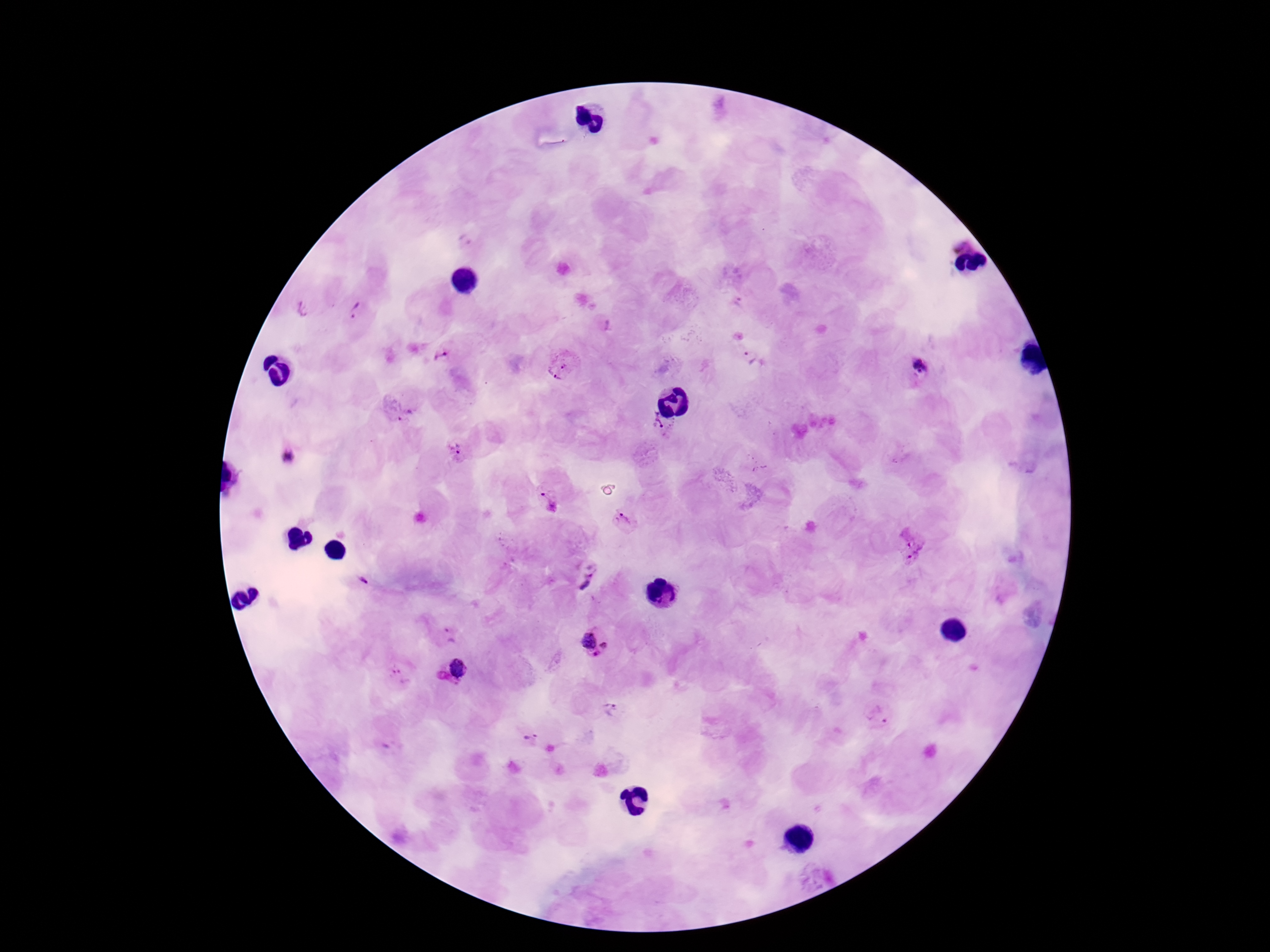 Approximate object centers, in pixels from the top-left corner. Plasmodium parasite locations: (x=357, y=312), (x=442, y=356), (x=753, y=358), (x=561, y=368), (x=920, y=369), (x=398, y=408), (x=659, y=426), (x=458, y=450), (x=288, y=457), (x=548, y=499), (x=625, y=521), (x=908, y=544), (x=588, y=577), (x=363, y=579), (x=448, y=633), (x=595, y=643), (x=455, y=671), (x=398, y=678), (x=610, y=708), (x=879, y=714), (x=532, y=737). Photographed through the microscope eyepiece with a smartphone camera. One field from this slide. Image is 1270×952 pixels. Giemsa-stained preparation. 100x magnification. Patient malaria status: infected. Thick blood film.